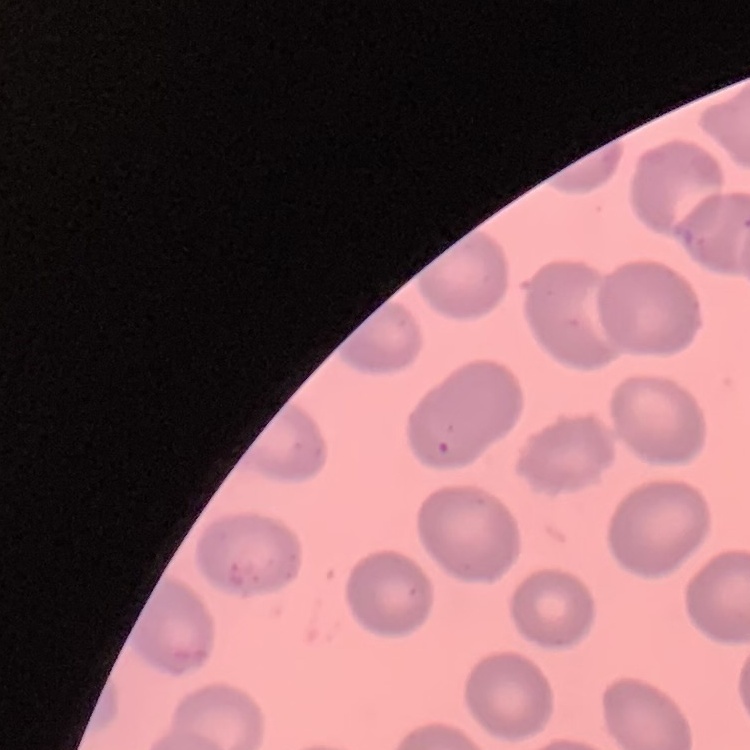 The erythrocytes exhibit no rouleaux formation. Thin peripheral smear. Square crop of a larger photomicrograph. Stained with either Field's or Giemsa.